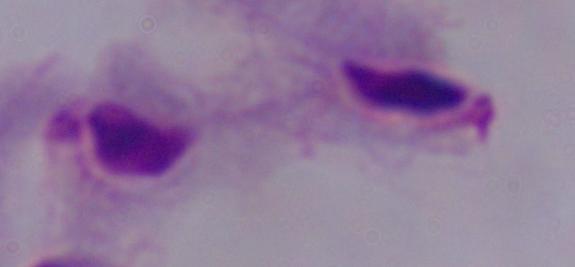

{
  "modality": "micrograph",
  "magnification": "1000x",
  "identification": "trichomonad"
}